Name the parasite shown.
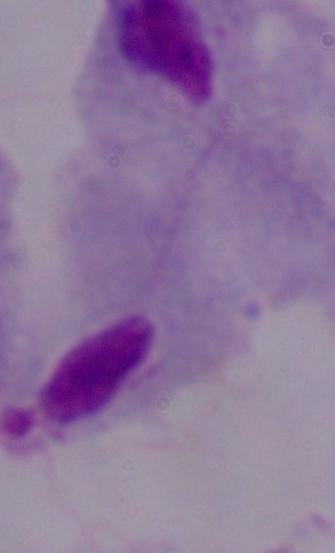

A trichomonad.

{
  "magnification": "1000x",
  "modality": "micrograph"
}